Identify the parasite.
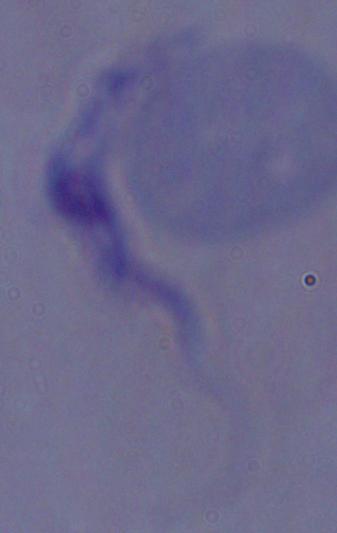
A trypanosome.

Summary:
  - Modality: micrograph
  - Magnification: 1000x